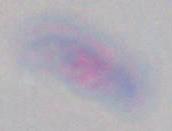

magnification = 1000x
modality = photomicrograph
identification = Toxoplasma gondii